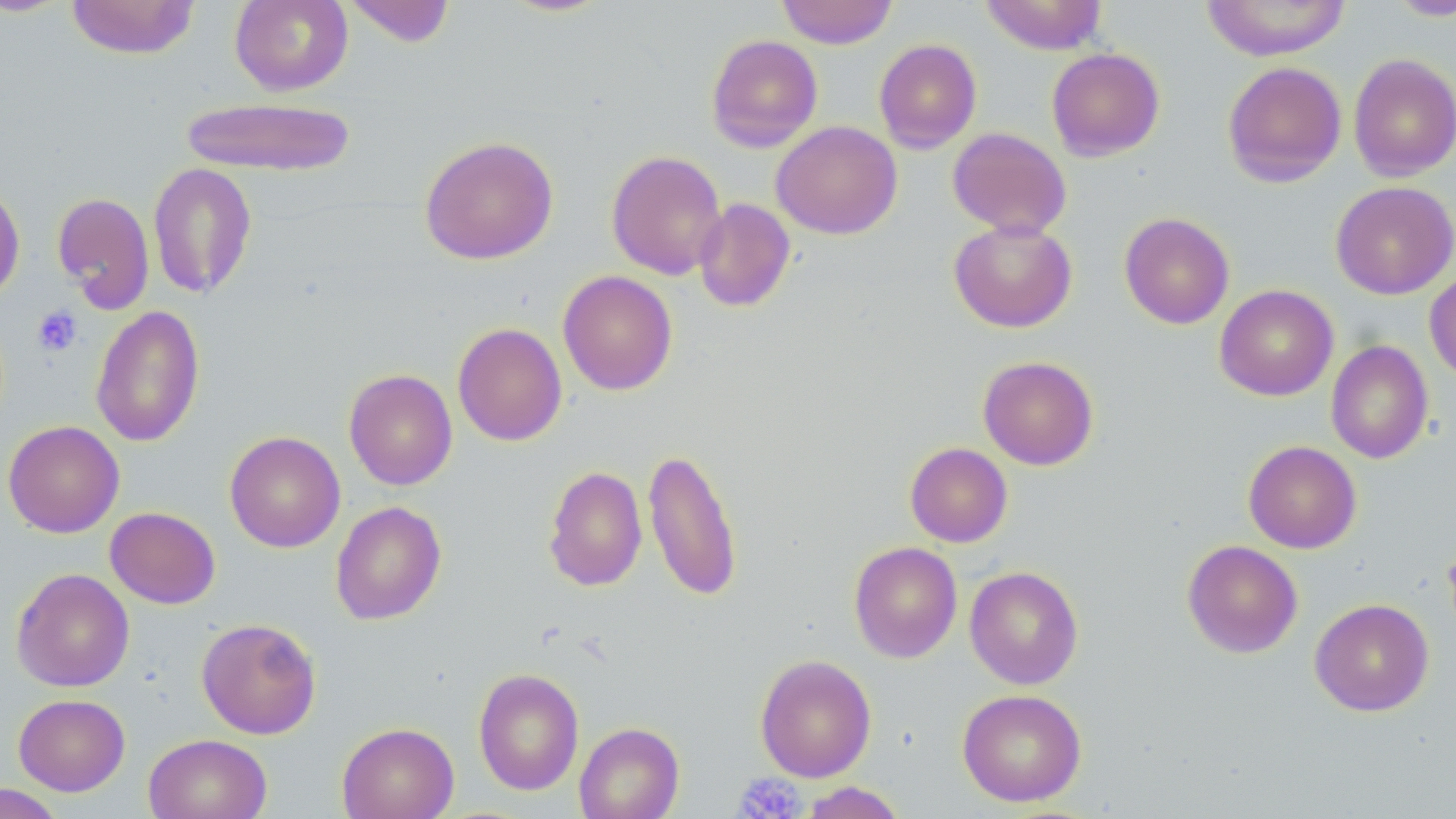

slide-level diagnosis = no evidence of blood parasites
modality = light microscopy
preparation = thin blood smear
stain = May-Grünwald-Giemsa
field of view = one of a larger specimen
image size = 1456×819 pixels
platelet locations = approximate bounding boxes as (x1, y1, x2, y2) in pixels: (32, 306, 83, 357), (734, 772, 806, 818)
uninfected red blood cell locations = approximate bounding boxes as (x1, y1, x2, y2) in pixels: (65, 0, 200, 59), (229, 0, 353, 96), (343, 0, 456, 47), (776, 0, 897, 49), (979, 0, 1108, 55), (1201, 0, 1352, 60), (1386, 0, 1456, 21), (706, 34, 823, 152), (873, 38, 982, 153), (1046, 48, 1165, 161), (1348, 53, 1456, 181), (1222, 61, 1347, 188), (179, 96, 358, 177), (771, 121, 902, 240), (947, 127, 1072, 239), (419, 135, 559, 265), (606, 150, 727, 280), (148, 161, 257, 300), (0, 180, 25, 304), (1330, 181, 1456, 300), (53, 192, 154, 313), (694, 198, 796, 312), (1119, 212, 1234, 329), (949, 219, 1077, 332), (1424, 268, 1456, 382), (557, 270, 678, 395), (1214, 284, 1338, 401), (91, 305, 205, 447), (452, 322, 567, 446), (1325, 340, 1433, 464), (978, 355, 1099, 470), (343, 368, 458, 490), (3, 420, 124, 537), (224, 431, 345, 553), (1243, 440, 1362, 554), (905, 442, 1013, 547), (642, 446, 744, 603), (543, 465, 647, 592), (330, 501, 447, 625), (105, 506, 220, 609), (1182, 539, 1303, 658), (849, 541, 962, 663), (964, 566, 1084, 689), (11, 567, 135, 692), (1309, 598, 1434, 716), (196, 617, 322, 740), (754, 654, 877, 782), (473, 667, 585, 796), (957, 688, 1087, 807), (13, 693, 130, 796), (574, 721, 685, 819), (336, 722, 459, 818), (143, 734, 272, 819), (799, 781, 907, 819), (0, 784, 66, 819)
magnification = 1000x